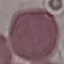

Summary:
  - Result: negative for malaria parasites
  - Capture: smartphone through the microscope eyepiece
  - Image type: automatically extracted cell patch, resized to 64 × 64 pixels
  - Preparation: thin blood smear
  - Stain: Giemsa